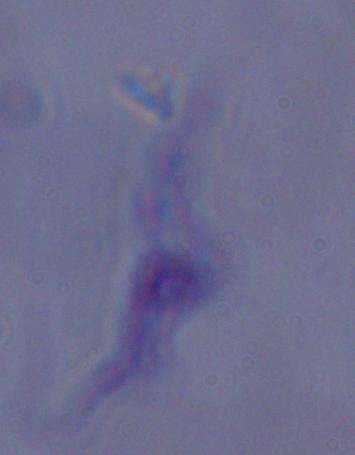
Summary:
  - Magnification: 1000x
  - Identification: trypanosome
  - Modality: photomicrograph